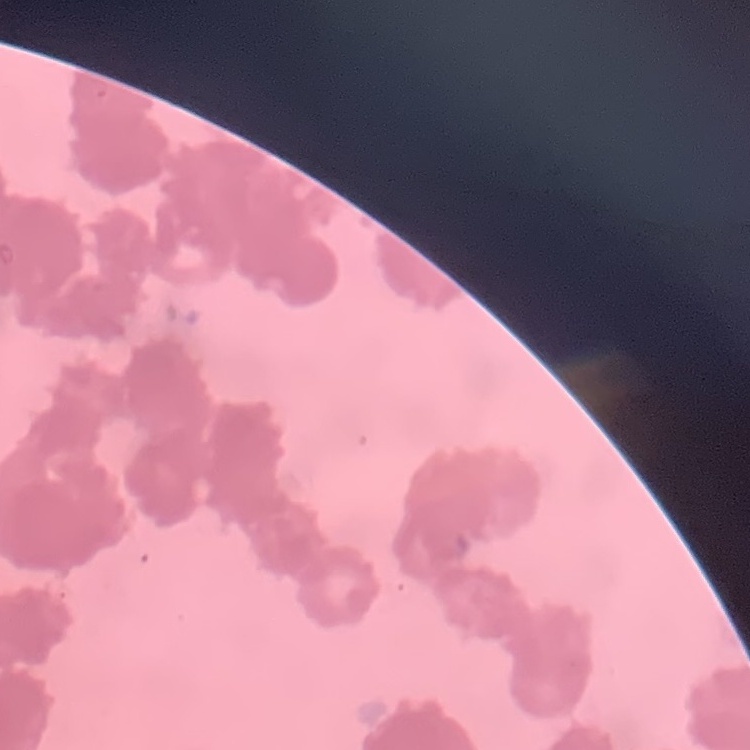

red blood cell morphology = rouleaux formation
image type = square crop of a larger photomicrograph
stain = Field's or Giemsa
preparation = thin blood smear